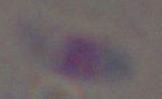

{
  "identification": "Toxoplasma gondii",
  "modality": "photomicrograph",
  "magnification": "1000x"
}